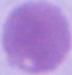

Summary:
  - Modality: photomicrograph
  - Identification: erythrocyte
  - Magnification: 1000x